Name the parasite shown.
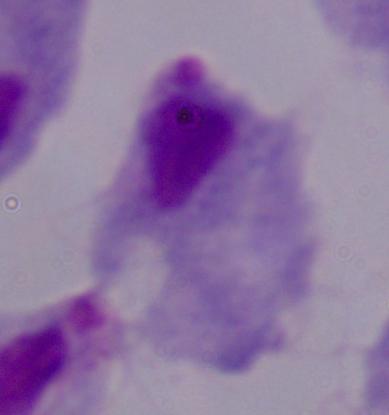

A trichomonad.

Captured at 1000x magnification. Photomicrograph.